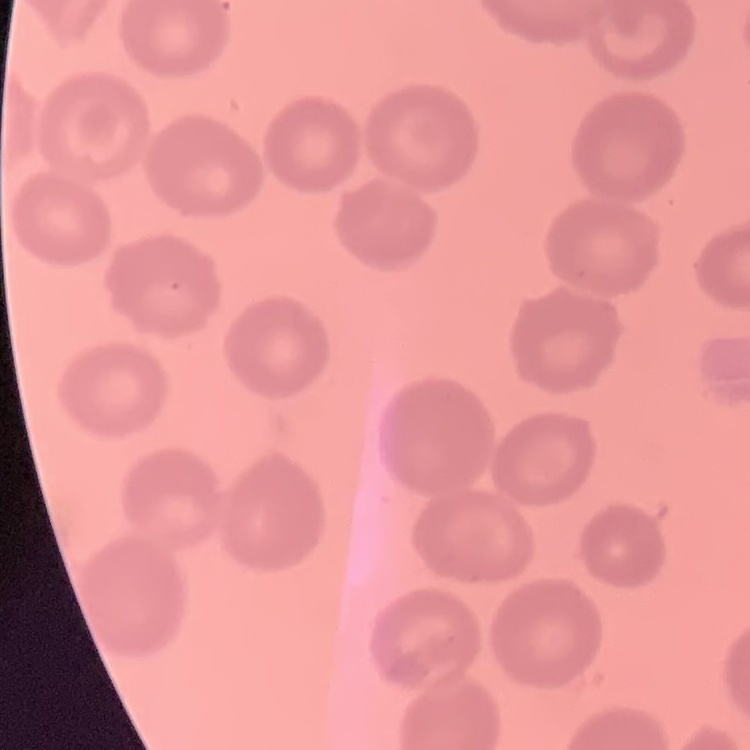

red blood cell morphology = no rouleaux formation
stain = Field's or Giemsa
preparation = thin peripheral smear
image type = square crop of a larger photomicrograph